Classify this cell by malaria status.
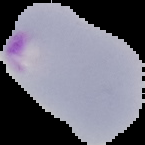
Parasitized.

image size = 145×145 pixels
preparation = thin blood smear
image type = cell region segmented out of the field of view; surrounding area masked to black